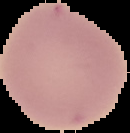
Summary:
  - Image type: cell region segmented out of the field of view; surrounding area masked to black
  - Malaria status: uninfected
  - Preparation: thin blood smear
  - Image size: 130×133 pixels